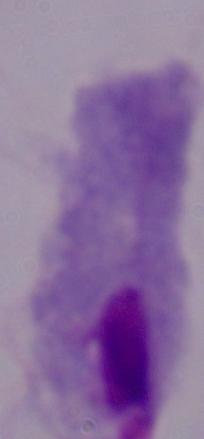
Photomicrograph. Captured at 1000x magnification. A trichomonad is shown.